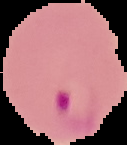 Image is 127×145 pixels. From a thin blood smear. The area outside the segmented cell region is set to black. Result: malaria parasites identified.